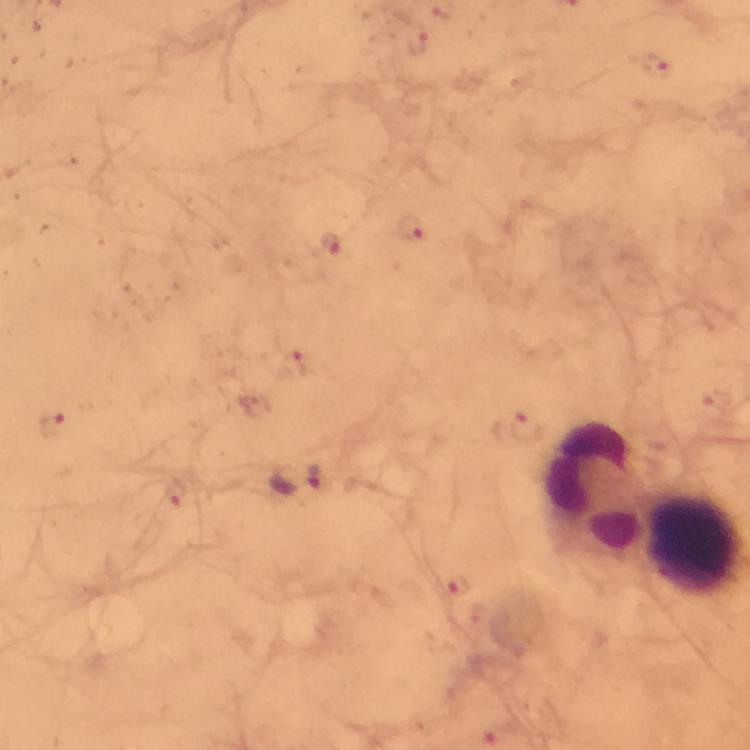

{
  "immersion_oil": "used",
  "magnification": "100x",
  "leukocyte_locations": "approximate object centers, in pixels from the top-left corner: (x=595, y=489), (x=696, y=544)",
  "context": "from a diagnostic examination for malaria",
  "cropped_from": "one field of view",
  "image_size": "750×750 pixels",
  "stain": "Giemsa",
  "capture": "smartphone camera through the microscope",
  "malaria_parasite_locations": "approximate object centers, in pixels from the top-left corner: (x=416, y=43), (x=411, y=230), (x=333, y=245), (x=298, y=478)",
  "preparation": "thick smear"
}